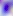

Summary:
  - Identification: Toxoplasma gondii
  - Magnification: 400x
  - Modality: photomicrograph